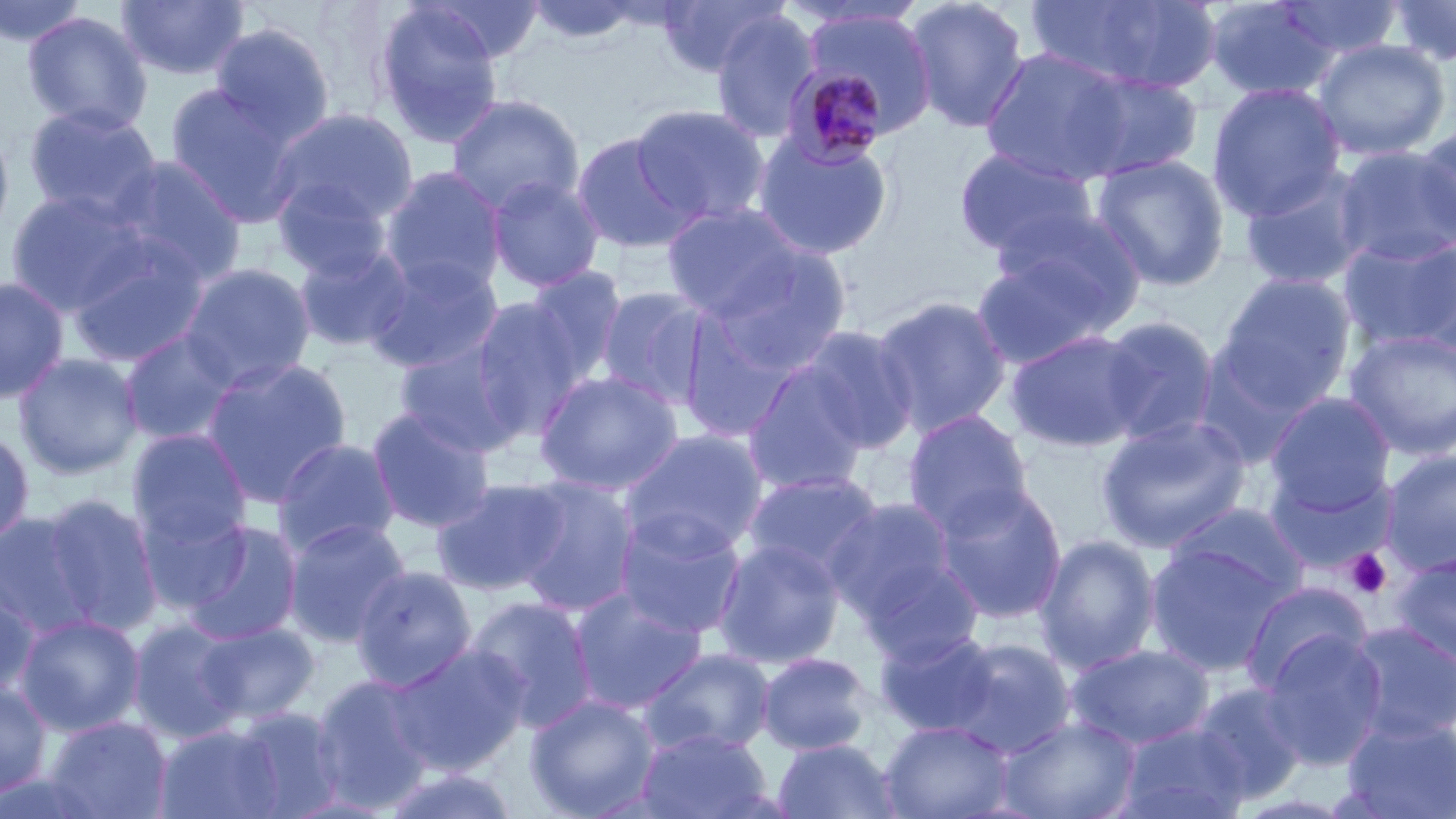

slide-level diagnosis = Plasmodium malariae
stain = May-Grünwald-Giemsa
field of view = single
image size = 1456×819 pixels
platelet locations = approximate bounding boxes as named x1/y1/x2/y2 corners in pixels: (x1=1344, y1=548, x2=1392, y2=599)
Plasmodium malariae-infected red blood cell locations = approximate bounding boxes as named x1/y1/x2/y2 corners in pixels: (x1=782, y1=62, x2=892, y2=168)
uninfected red blood cell locations = approximate bounding boxes as named x1/y1/x2/y2 corners in pixels: (x1=420, y1=0, x2=546, y2=63), (x1=526, y1=0, x2=643, y2=44), (x1=656, y1=0, x2=786, y2=77), (x1=904, y1=0, x2=1031, y2=134), (x1=1024, y1=0, x2=1221, y2=93), (x1=1202, y1=0, x2=1338, y2=102), (x1=1274, y1=0, x2=1404, y2=60), (x1=1384, y1=0, x2=1456, y2=67), (x1=0, y1=1, x2=91, y2=47), (x1=116, y1=1, x2=250, y2=81), (x1=372, y1=2, x2=506, y2=149), (x1=801, y1=9, x2=937, y2=136), (x1=709, y1=10, x2=820, y2=143), (x1=21, y1=11, x2=154, y2=135), (x1=210, y1=22, x2=336, y2=148), (x1=1311, y1=39, x2=1450, y2=161), (x1=979, y1=46, x2=1136, y2=186), (x1=1067, y1=70, x2=1204, y2=181), (x1=166, y1=82, x2=303, y2=226), (x1=1207, y1=82, x2=1347, y2=221), (x1=446, y1=94, x2=585, y2=217), (x1=24, y1=104, x2=162, y2=223), (x1=629, y1=104, x2=770, y2=226), (x1=268, y1=107, x2=419, y2=236), (x1=0, y1=120, x2=15, y2=249), (x1=1415, y1=122, x2=1455, y2=243), (x1=570, y1=131, x2=699, y2=254), (x1=752, y1=132, x2=894, y2=261), (x1=1331, y1=144, x2=1456, y2=267), (x1=953, y1=146, x2=1100, y2=260), (x1=1091, y1=154, x2=1230, y2=291), (x1=108, y1=156, x2=247, y2=286), (x1=1238, y1=164, x2=1373, y2=291), (x1=380, y1=166, x2=507, y2=295), (x1=272, y1=175, x2=395, y2=282), (x1=484, y1=175, x2=606, y2=293), (x1=6, y1=190, x2=151, y2=316), (x1=661, y1=203, x2=809, y2=322), (x1=988, y1=206, x2=1146, y2=331), (x1=1338, y1=234, x2=1456, y2=354), (x1=66, y1=235, x2=212, y2=368), (x1=293, y1=241, x2=414, y2=354), (x1=705, y1=243, x2=854, y2=378), (x1=1408, y1=244, x2=1456, y2=354), (x1=363, y1=253, x2=504, y2=374), (x1=973, y1=254, x2=1118, y2=370), (x1=179, y1=263, x2=317, y2=390), (x1=523, y1=266, x2=628, y2=384), (x1=1213, y1=272, x2=1357, y2=414), (x1=0, y1=275, x2=70, y2=406), (x1=596, y1=287, x2=710, y2=408), (x1=871, y1=295, x2=1013, y2=439), (x1=466, y1=297, x2=588, y2=439), (x1=1096, y1=316, x2=1220, y2=446), (x1=795, y1=326, x2=919, y2=455), (x1=1344, y1=328, x2=1456, y2=462), (x1=1005, y1=329, x2=1148, y2=452), (x1=119, y1=330, x2=241, y2=447), (x1=393, y1=339, x2=526, y2=458), (x1=12, y1=352, x2=144, y2=480), (x1=201, y1=357, x2=353, y2=508), (x1=743, y1=363, x2=872, y2=496), (x1=534, y1=370, x2=684, y2=496), (x1=1264, y1=393, x2=1396, y2=515), (x1=365, y1=405, x2=496, y2=533), (x1=902, y1=409, x2=1034, y2=537), (x1=1096, y1=415, x2=1252, y2=555), (x1=0, y1=427, x2=35, y2=549), (x1=620, y1=428, x2=769, y2=556), (x1=128, y1=430, x2=251, y2=549), (x1=272, y1=438, x2=401, y2=558), (x1=1379, y1=449, x2=1456, y2=576), (x1=1262, y1=460, x2=1395, y2=575), (x1=742, y1=471, x2=884, y2=586), (x1=512, y1=477, x2=640, y2=618), (x1=431, y1=478, x2=569, y2=596), (x1=933, y1=481, x2=1068, y2=624), (x1=40, y1=493, x2=164, y2=635), (x1=825, y1=495, x2=965, y2=635), (x1=135, y1=500, x2=252, y2=615), (x1=1166, y1=502, x2=1311, y2=605), (x1=614, y1=509, x2=747, y2=639), (x1=0, y1=510, x2=102, y2=639), (x1=284, y1=517, x2=411, y2=647), (x1=180, y1=520, x2=305, y2=645), (x1=1035, y1=534, x2=1160, y2=675), (x1=712, y1=538, x2=845, y2=669), (x1=1146, y1=543, x2=1287, y2=676), (x1=1389, y1=551, x2=1456, y2=667), (x1=351, y1=565, x2=477, y2=692), (x1=0, y1=581, x2=41, y2=699), (x1=1239, y1=581, x2=1372, y2=696), (x1=568, y1=587, x2=707, y2=714), (x1=464, y1=596, x2=598, y2=731), (x1=15, y1=613, x2=145, y2=737), (x1=128, y1=618, x2=245, y2=743), (x1=195, y1=621, x2=318, y2=726), (x1=1345, y1=621, x2=1456, y2=745), (x1=875, y1=629, x2=1003, y2=738), (x1=1260, y1=630, x2=1388, y2=770), (x1=940, y1=637, x2=1075, y2=757), (x1=385, y1=643, x2=531, y2=776), (x1=1066, y1=643, x2=1214, y2=750), (x1=639, y1=648, x2=775, y2=757), (x1=757, y1=652, x2=874, y2=756), (x1=311, y1=673, x2=435, y2=812), (x1=0, y1=681, x2=53, y2=799), (x1=1190, y1=682, x2=1309, y2=803), (x1=525, y1=694, x2=661, y2=819), (x1=231, y1=707, x2=346, y2=818), (x1=1340, y1=714, x2=1456, y2=819), (x1=44, y1=715, x2=172, y2=819), (x1=997, y1=715, x2=1140, y2=819), (x1=880, y1=720, x2=1014, y2=819), (x1=1117, y1=722, x2=1252, y2=819), (x1=155, y1=723, x2=285, y2=819), (x1=637, y1=728, x2=773, y2=819), (x1=773, y1=738, x2=901, y2=819), (x1=378, y1=766, x2=522, y2=819)
modality = optical microscopy
preparation = thin blood smear
magnification = 1000x